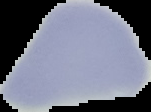
Summary:
  - Image type: cell region segmented out of the field of view; surrounding area masked to black
  - Preparation: thin blood film
  - Image size: 151×112 pixels
  - Result: no malaria parasites seen